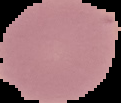

Summary:
  - Image type: segmented cell region on a black background
  - Preparation: thin blood smear
  - Image size: 121×103 pixels
  - Result: negative for Plasmodium parasites